Classify this cell by malaria status.
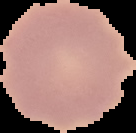
Uninfected.

Summary:
  - Preparation: thin blood film
  - Image size: 136×133 pixels
  - Image type: segmented cell region with the area outside set to black